Comment on the morphology of the red blood cells.
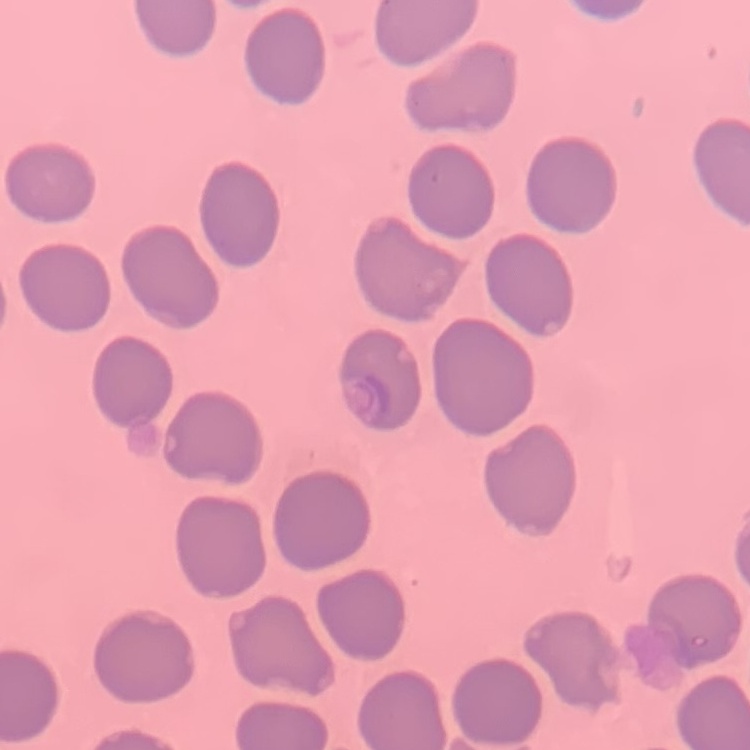
No rouleaux formation.

stain = Field's or Giemsa
preparation = thin blood smear
image type = square crop of a larger photomicrograph